Outline malaria parasites and classify them by life-cycle stage.
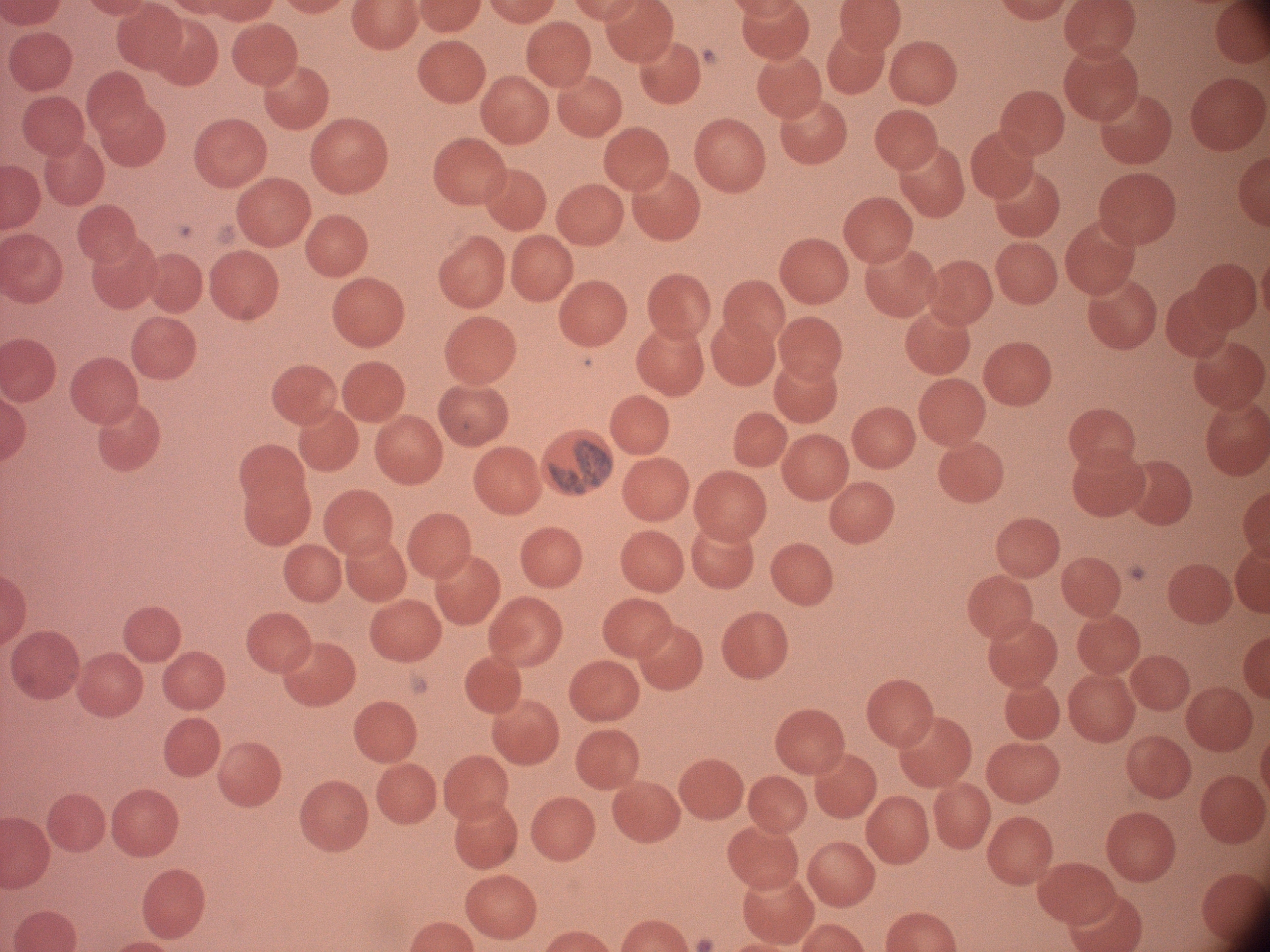
Approximate bounding boxes as [x1, y1, x2, y2] in pixels, from the source annotation, which is not necessarily exhaustive.
Gametocytes: [548, 440, 612, 494].

Summary:
  - Microscope: Leica DM2000 with built-in camera
  - Field of view: single
  - Image size: 1270×952 pixels
  - Preparation: thin blood film
  - Species: Plasmodium malariae
  - Magnification: 100x
  - Stain: Giemsa